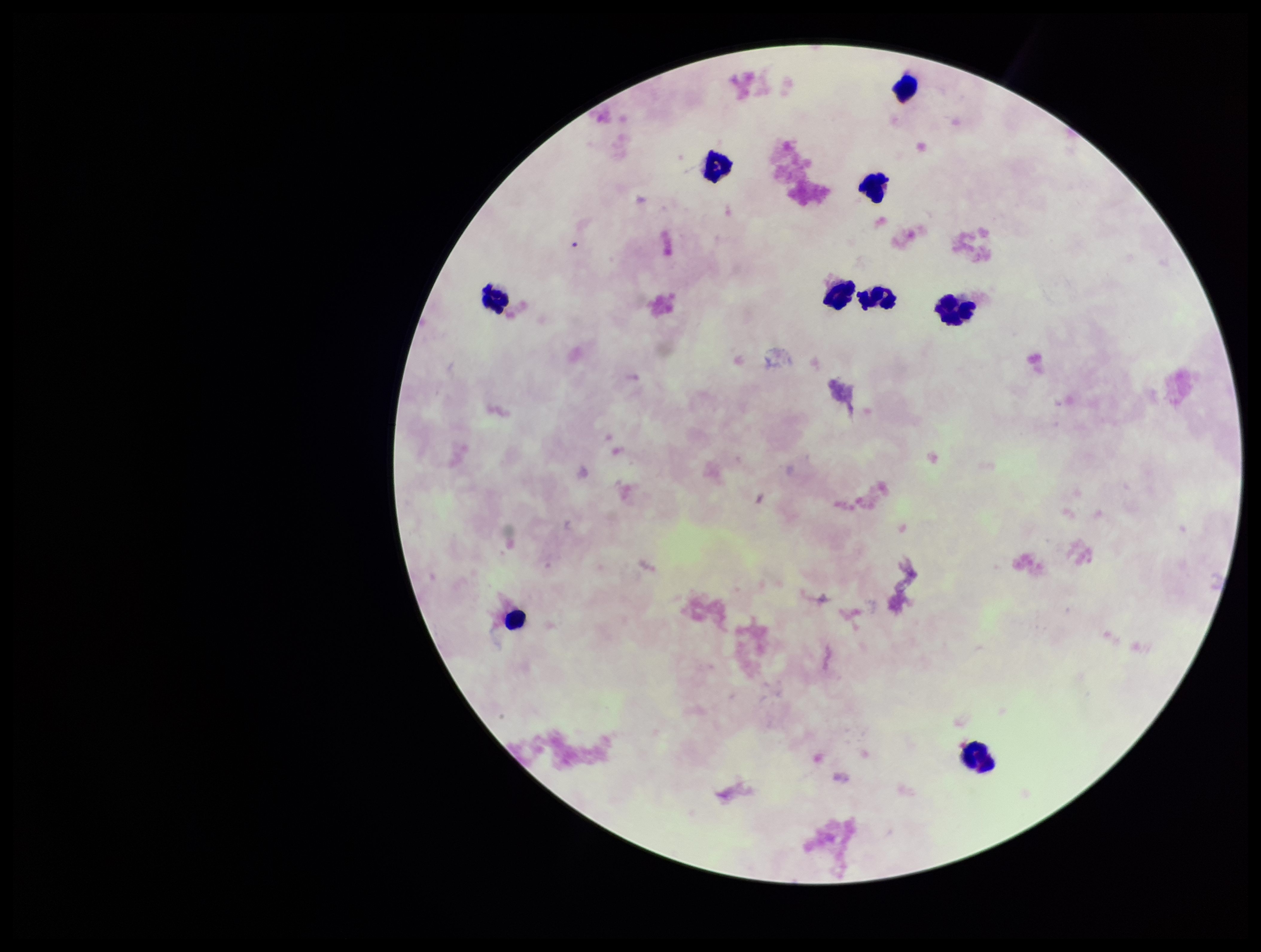
Summary:
  - Field of view: single
  - Image size: 1261×952 pixels
  - Plasmodium parasites: none seen
  - Capture: smartphone photograph through the microscope eyepiece
  - Preparation: thick blood smear
  - Stain: Giemsa
  - Patient malaria status: negative
  - Parasite count: 0
  - Leukocyte count: 9